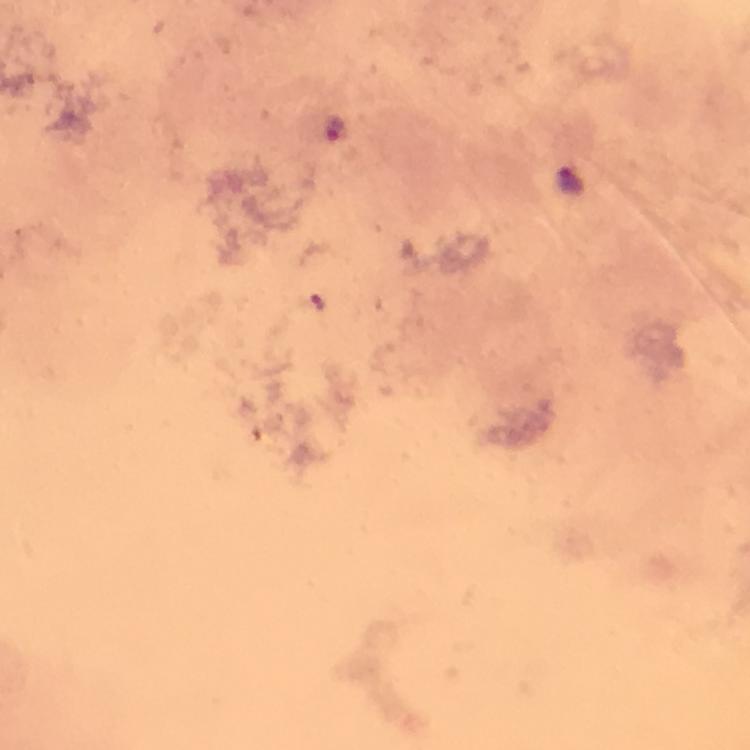 Approximate centers as {x, y} in pixels. Plasmodium parasite locations: {335, 128}, {570, 180}. Image is 750×750 pixels. A crop from one field of view. 100x magnification. From a malaria diagnostic workup. Thick blood smear. Immersion oil was used. Giemsa stain. Smartphone photograph taken through a microscope.